Identify the parasite.
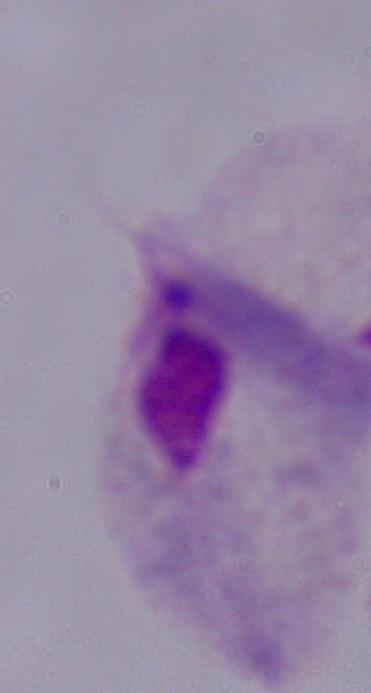
This is a trichomonad.

Summary:
  - Magnification: 1000x
  - Modality: micrograph